Classify this cell by malaria status.
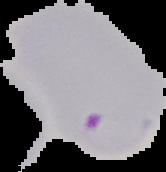

Parasitized.

Segmented cell region on a black background. From a thin blood smear. Image is 166×172 pixels.